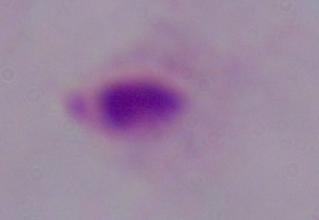

magnification = 1000x
identification = trichomonad
modality = micrograph